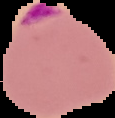
Summary:
  - Image type: segmented cell region with the area outside set to black
  - Preparation: thin blood smear
  - Image size: 115×118 pixels
  - Result: malaria parasites identified